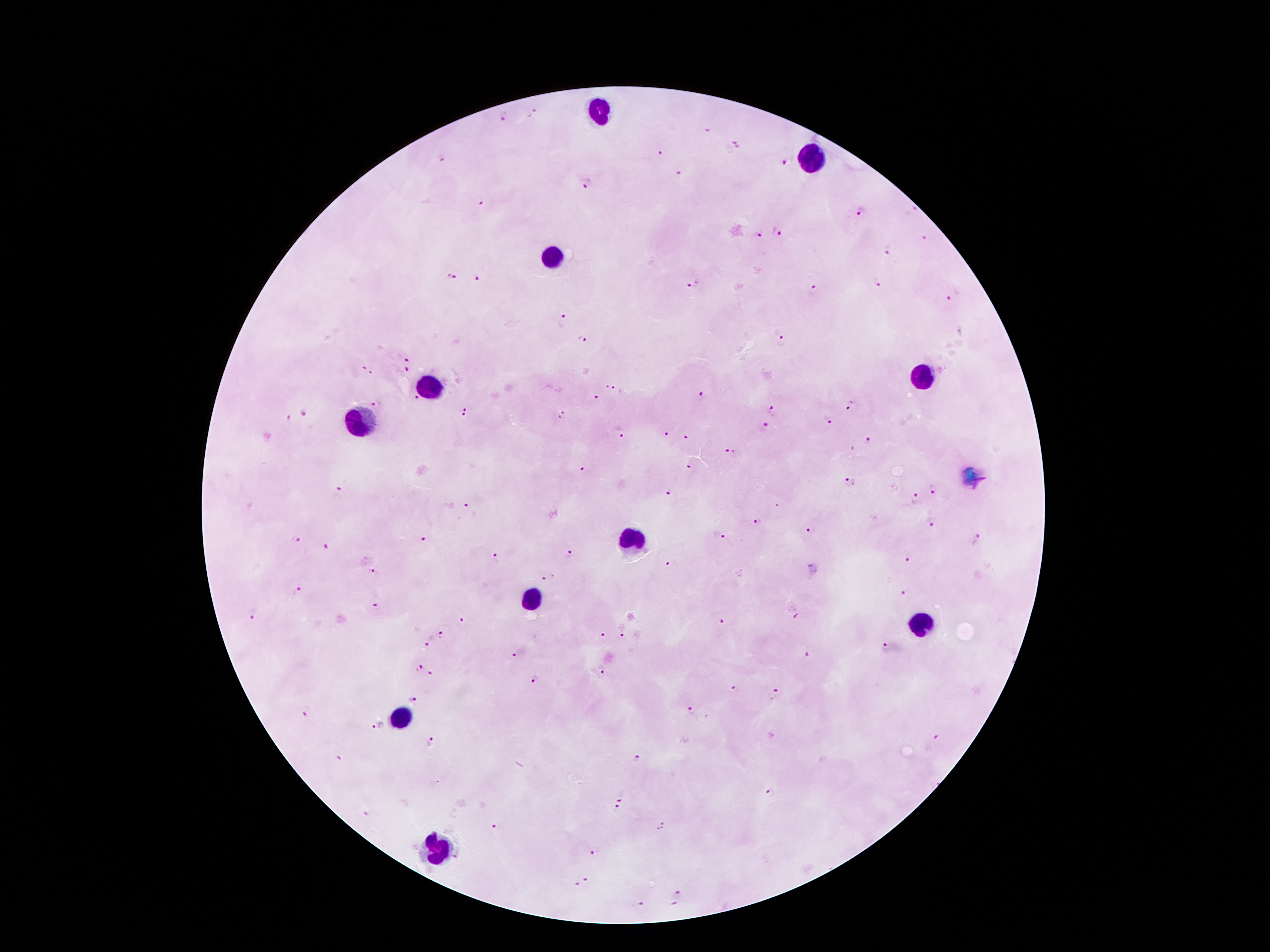

Approximate centers as {x, y} in pixels. Leukocyte locations: {598, 113}, {809, 158}, {553, 257}, {922, 379}, {425, 388}, {361, 425}, {633, 539}, {534, 602}, {919, 622}, {399, 720}, {439, 849}. Plasmodium parasite locations: {503, 115}, {532, 115}, {706, 130}, {736, 146}, {661, 152}, {442, 160}, {787, 161}, {680, 175}, {587, 184}, {482, 200}, {861, 211}, {777, 231}, {757, 235}, {924, 237}, {887, 250}, {451, 277}, {479, 280}, {692, 285}, {876, 285}, {814, 290}, {953, 297}, {563, 321}, {582, 337}, {783, 340}, {409, 358}, {363, 365}, {408, 369}, {372, 374}, {607, 386}, {617, 390}, {414, 395}, {704, 397}, {596, 398}, {375, 404}, {848, 404}, {772, 410}, {305, 412}, {465, 412}, {561, 416}, {286, 418}, {826, 421}, {765, 425}, {666, 432}, {621, 433}, {687, 437}, {867, 441}, {729, 451}, {690, 466}, {581, 469}, {849, 482}, {933, 488}, {337, 490}, {668, 492}, {914, 499}, {467, 506}, {778, 506}, {757, 521}, {931, 521}, {810, 530}, {718, 535}, {296, 538}, {977, 539}, {423, 540}, {325, 546}, {570, 556}, {909, 558}, {494, 559}, {671, 561}, {372, 571}, {548, 578}, {297, 592}, {902, 594}, {377, 607}, {252, 616}, {797, 616}, {463, 621}, {721, 624}, {601, 635}, {622, 636}, {441, 637}, {429, 640}, {887, 647}, {513, 655}, {806, 657}, {420, 668}, {600, 670}, {432, 675}, {533, 679}, {735, 688}, {776, 693}, {413, 699}, {309, 711}, {690, 711}, {378, 726}, {430, 740}, {936, 740}, {340, 758}, {636, 758}, {770, 792}, {621, 795}, {615, 811}, {494, 827}, {592, 852}, {585, 880}, {574, 886}, {678, 893}, {638, 905}. Smartphone photograph taken through the microscope eyepiece. 100x magnification. Thick peripheral-blood smear. Giemsa stain. Single field of view. Patient malaria status: positive for Plasmodium falciparum. Image is 1270×952 pixels.